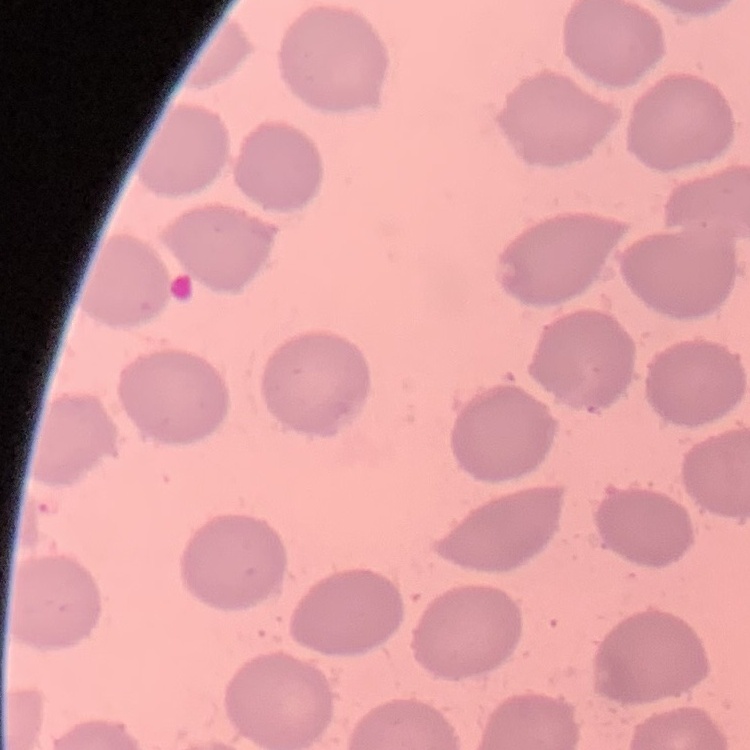

The erythrocytes exhibit no rouleaux formation. Thin blood smear. Stained with either Field's or Giemsa. Square crop of a larger photomicrograph.